Identify the blood parasite species.
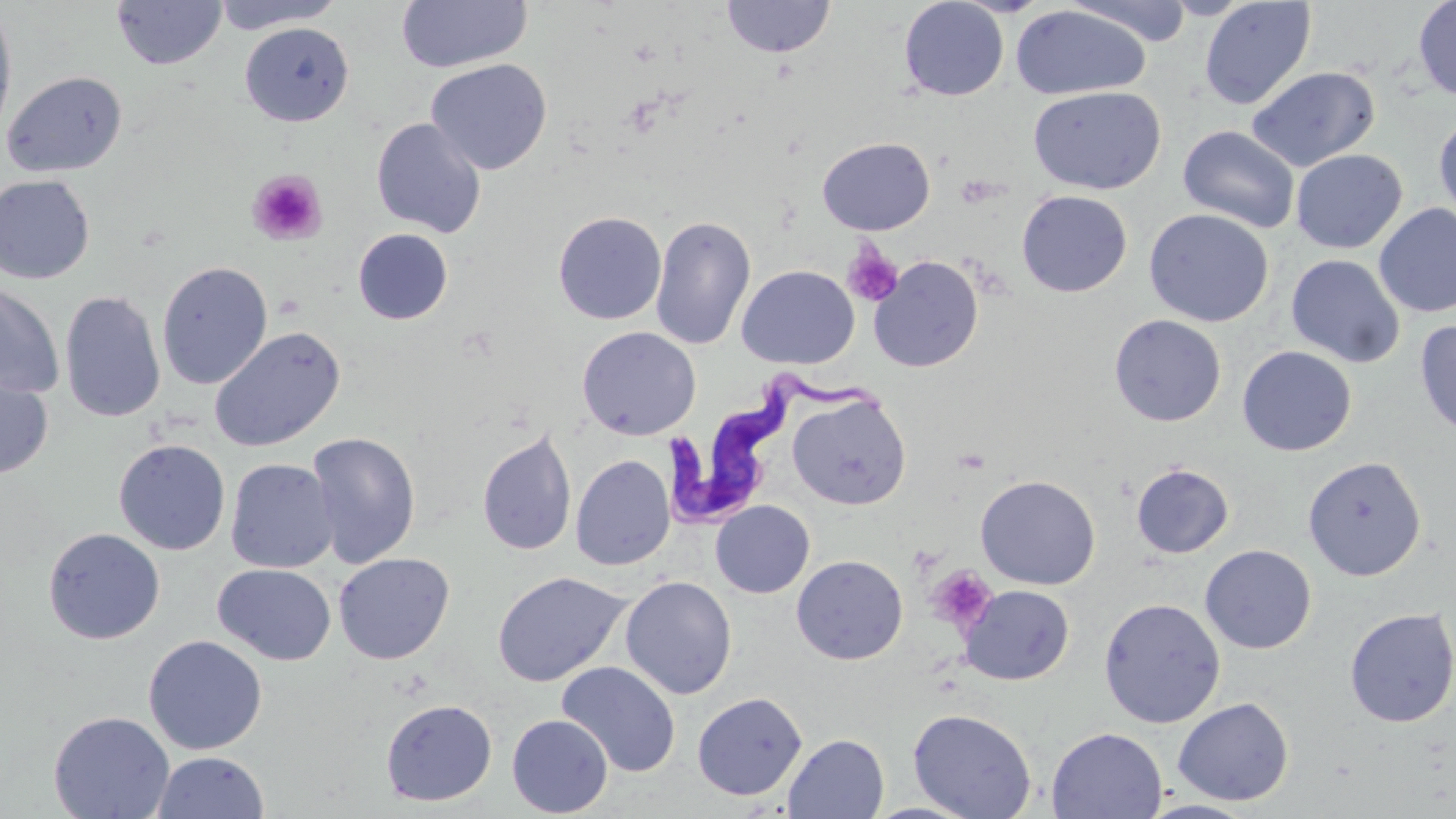
Trypanosoma brucei.

Summary:
  - Coordinate format: approximate bounding boxes as (x1,y1)-(x2,y2) corner pairs in pixels
  - Trypanosoma brucei locations: (669,369)-(889,525)
  - Uninfected red blood cell locations: (210,0)-(347,33), (396,0)-(531,74), (722,0)-(836,59), (898,0)-(1009,101), (1064,0)-(1196,47), (1199,0)-(1317,110), (1412,0)-(1456,103), (111,1)-(226,71), (0,4)-(17,147), (1010,5)-(1151,100), (240,22)-(354,126), (426,59)-(552,175), (1246,65)-(1380,172), (2,70)-(128,179), (1027,85)-(1166,195), (1433,111)-(1456,227), (371,117)-(487,238), (1177,124)-(1300,233), (817,136)-(935,235), (1290,148)-(1408,254), (0,174)-(95,284), (1016,190)-(1133,297), (1374,203)-(1456,319), (1144,208)-(1274,327), (553,211)-(667,324), (650,215)-(757,351), (353,228)-(453,325), (1285,253)-(1406,368), (867,255)-(984,373), (157,261)-(273,389), (737,265)-(859,369), (0,282)-(64,399), (59,290)-(166,423), (1108,314)-(1227,426), (1414,319)-(1456,439), (209,326)-(346,453), (577,326)-(701,440), (1237,345)-(1357,457), (0,369)-(54,481), (787,391)-(911,510), (476,428)-(577,557), (307,432)-(421,569), (113,439)-(231,555), (571,454)-(675,571), (1302,456)-(1427,580), (225,458)-(339,574), (1130,463)-(1234,559), (975,474)-(1101,590), (710,500)-(815,598), (42,527)-(165,644), (1199,544)-(1317,654), (333,552)-(455,665), (791,555)-(908,665), (212,563)-(336,666), (492,571)-(630,687), (620,576)-(737,700), (958,584)-(1074,685), (1098,597)-(1226,727), (1344,606)-(1456,728), (143,635)-(267,755), (556,662)-(681,777), (692,692)-(807,800), (1172,697)-(1294,806), (380,698)-(498,806), (908,707)-(1037,819), (48,710)-(175,819), (506,714)-(613,817), (1046,726)-(1167,818), (783,733)-(889,818), (152,751)-(270,819), (1140,800)-(1259,819)
  - Platelet locations: (246,169)-(327,246), (842,244)-(904,308), (927,565)-(998,632)
  - Preparation: thin blood film
  - Stain: May-Grünwald-Giemsa
  - Image size: 1456×819 pixels
  - Field of view: single
  - Modality: light microscopy
  - Magnification: 1000x